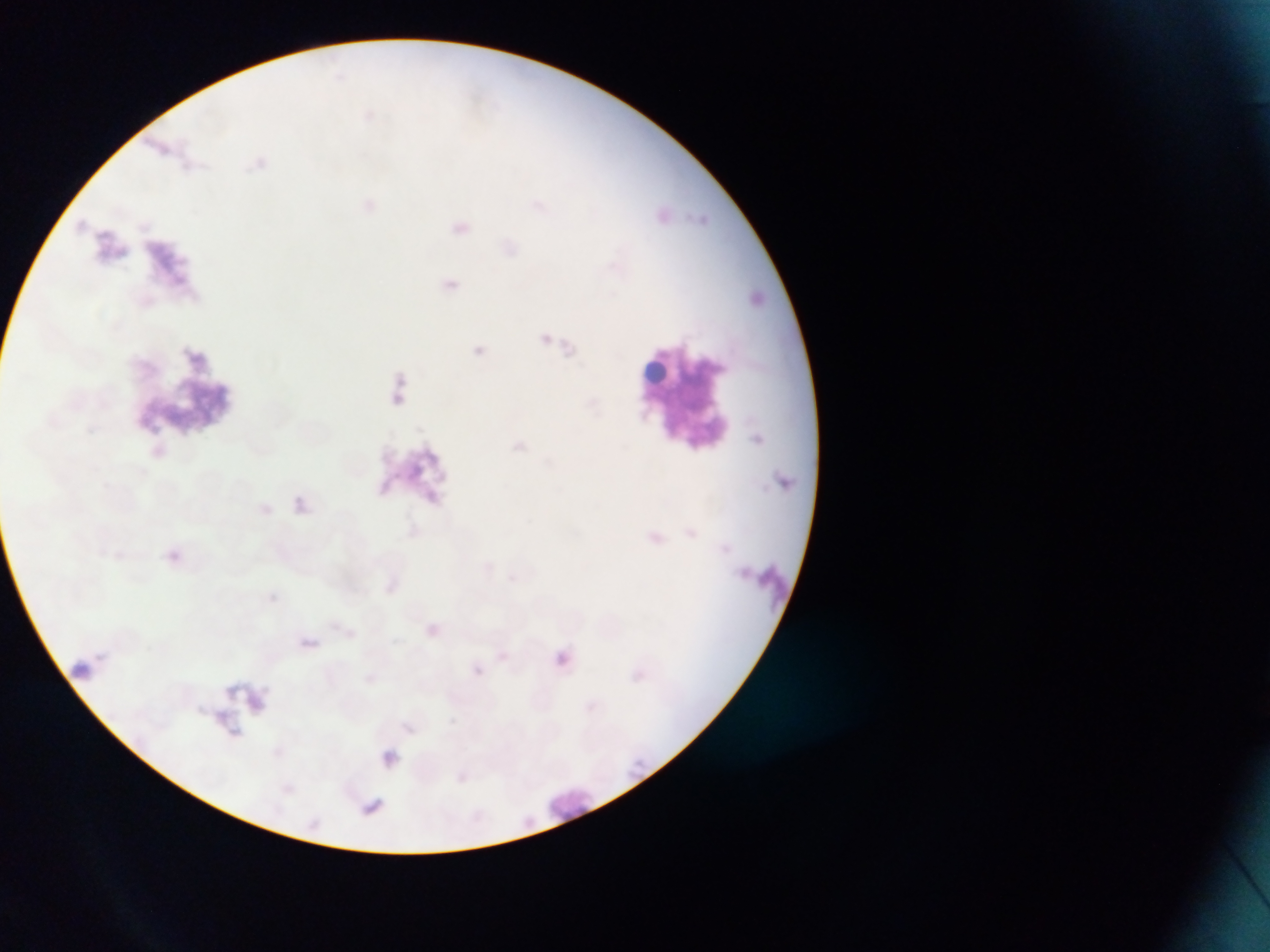

Approximate bounding boxes as [left, top, right, bottom] in pixels.
Summary:
  - Plasmodium parasite locations: [437, 276, 463, 301], [638, 524, 669, 553], [157, 543, 191, 574], [418, 619, 443, 642], [373, 744, 405, 773], [360, 791, 391, 821]
  - Artifact (stain precipitate or debris) locations: [145, 221, 201, 289], [628, 336, 748, 456], [121, 344, 243, 431], [365, 434, 451, 517], [735, 555, 799, 614], [72, 642, 99, 685], [222, 669, 283, 731]
  - Country: Ghana
  - Capture: mobile-phone photograph through a microscope
  - Preparation: thin blood film
  - Image size: 1270×952 pixels
  - Field of view: single